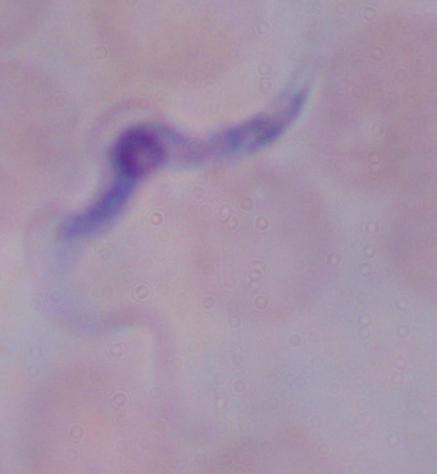

modality = micrograph
magnification = 1000x
identification = trypanosome